Identify the cell.
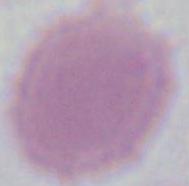

An erythrocyte.

1000x magnification. Photomicrograph.